State which parasite is depicted.
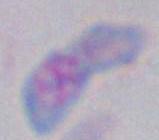

This is Toxoplasma gondii.

Summary:
  - Modality: photomicrograph
  - Magnification: 1000x